Describe the morphology of the red blood cells.
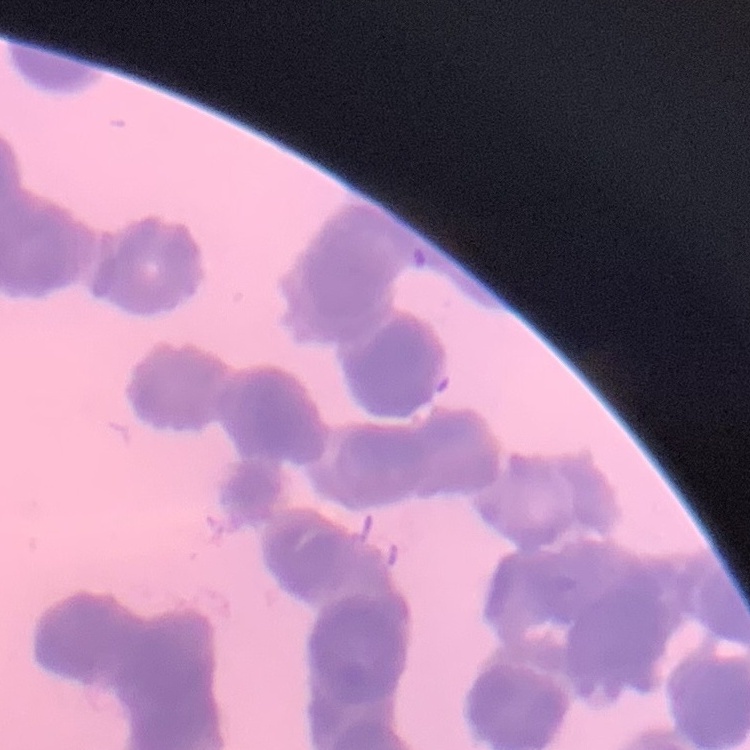
Rouleaux formation.

Field's or Giemsa stain. Thin blood film. Square crop of a larger photomicrograph.